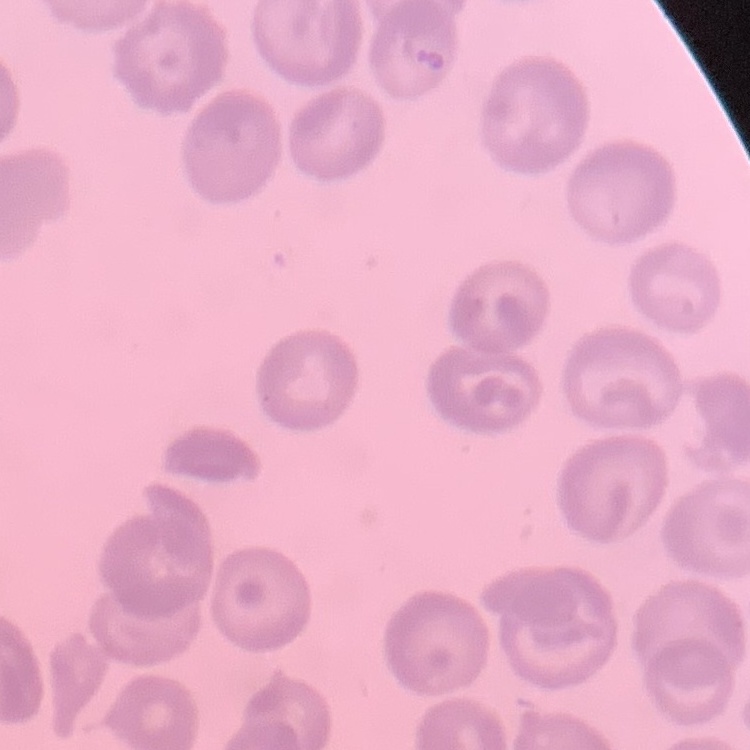

Summary:
  - Erythrocyte morphology: no rouleaux formation
  - Preparation: thin blood smear
  - Stain: Field's or Giemsa
  - Image type: square crop of a larger photomicrograph